Name the parasite shown.
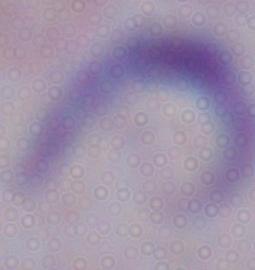
This is a trypanosome.

Summary:
  - Modality: photomicrograph
  - Magnification: 1000x